Assess this cell for malaria.
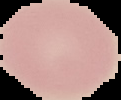

It is uninfected.

preparation = thin blood film
image type = segmented cell region with the area outside set to black
image size = 121×100 pixels